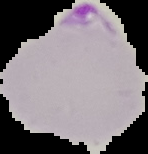
Summary:
  - Preparation: thin blood smear
  - Image type: segmented cell region on a black background
  - Image size: 148×154 pixels
  - Malaria status: parasitized